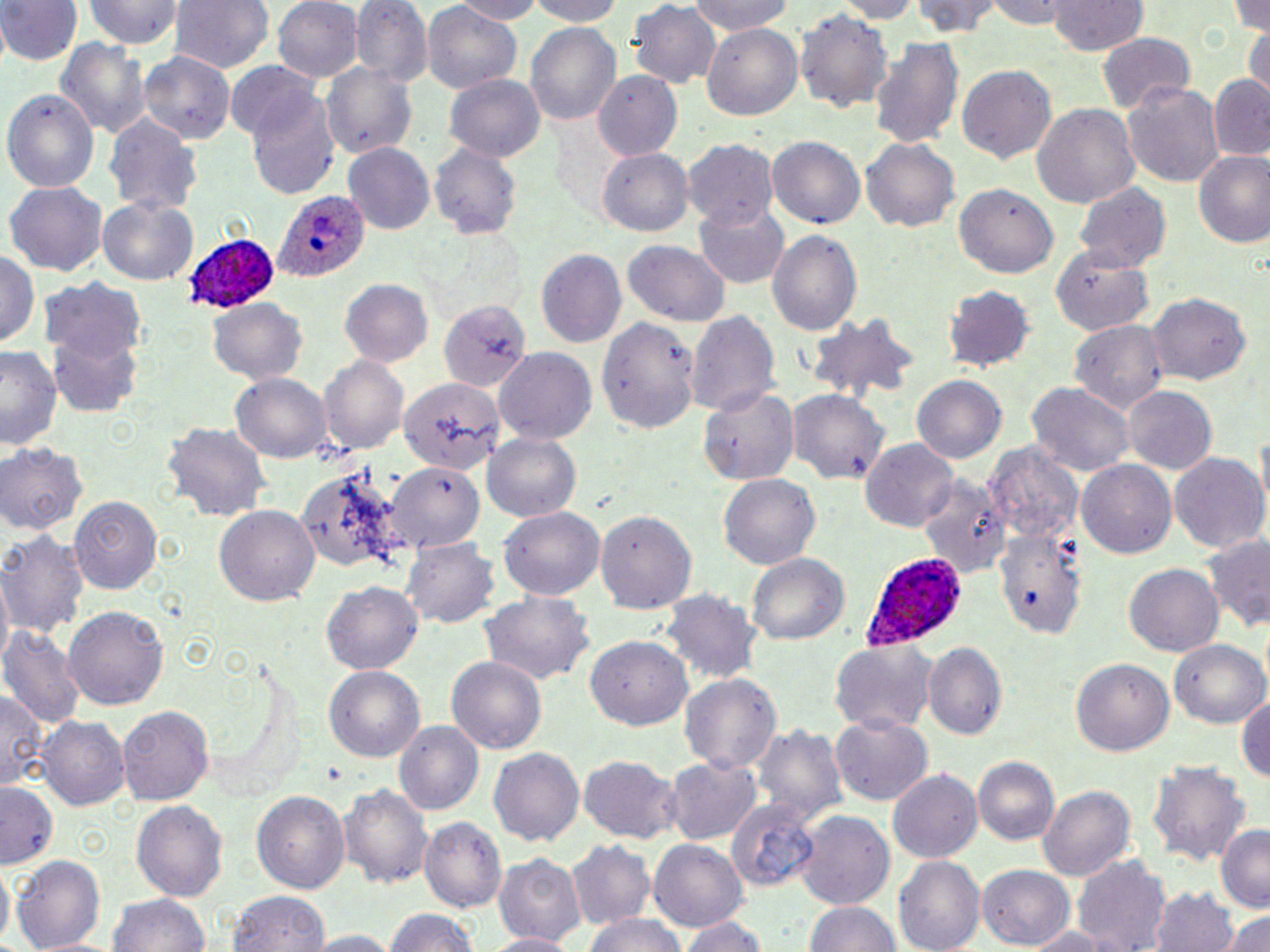
{
  "slide_level_diagnosis": "Plasmodium ovale",
  "field_of_view": "one of a larger specimen",
  "stain": "May-Grünwald-Giemsa",
  "uninfected_red_blood_cell_locations": "approximate bounding boxes as named x1/y1/x2/y2 corners in pixels: (x1=0, y1=0, x2=81, y2=67), (x1=171, y1=0, x2=274, y2=76), (x1=272, y1=0, x2=364, y2=85), (x1=351, y1=0, x2=432, y2=90), (x1=449, y1=0, x2=550, y2=23), (x1=525, y1=0, x2=632, y2=25), (x1=687, y1=0, x2=797, y2=35), (x1=828, y1=0, x2=925, y2=22), (x1=912, y1=0, x2=1003, y2=36), (x1=978, y1=0, x2=1072, y2=27), (x1=1049, y1=0, x2=1148, y2=57), (x1=1230, y1=0, x2=1270, y2=36), (x1=83, y1=1, x2=180, y2=50), (x1=422, y1=1, x2=522, y2=94), (x1=629, y1=1, x2=721, y2=91), (x1=794, y1=8, x2=894, y2=112), (x1=526, y1=22, x2=621, y2=123), (x1=1245, y1=23, x2=1270, y2=95), (x1=703, y1=25, x2=803, y2=119), (x1=1095, y1=33, x2=1196, y2=116), (x1=869, y1=36, x2=965, y2=150), (x1=56, y1=38, x2=153, y2=142), (x1=139, y1=50, x2=236, y2=144), (x1=226, y1=63, x2=325, y2=146), (x1=322, y1=65, x2=417, y2=158), (x1=957, y1=66, x2=1057, y2=164), (x1=594, y1=70, x2=681, y2=160), (x1=446, y1=73, x2=546, y2=161), (x1=1209, y1=77, x2=1270, y2=161), (x1=245, y1=82, x2=339, y2=199), (x1=1123, y1=83, x2=1226, y2=186), (x1=4, y1=89, x2=99, y2=194), (x1=1031, y1=102, x2=1140, y2=212), (x1=106, y1=115, x2=203, y2=217), (x1=766, y1=138, x2=864, y2=229), (x1=861, y1=138, x2=959, y2=230), (x1=683, y1=140, x2=776, y2=226), (x1=428, y1=141, x2=524, y2=242), (x1=342, y1=143, x2=435, y2=236), (x1=598, y1=150, x2=691, y2=235), (x1=1192, y1=150, x2=1270, y2=251), (x1=1073, y1=181, x2=1171, y2=271), (x1=6, y1=183, x2=106, y2=276), (x1=954, y1=184, x2=1058, y2=278), (x1=694, y1=197, x2=789, y2=287), (x1=99, y1=199, x2=197, y2=285), (x1=769, y1=228, x2=862, y2=338), (x1=622, y1=239, x2=730, y2=325), (x1=0, y1=247, x2=38, y2=352), (x1=1051, y1=249, x2=1152, y2=335), (x1=536, y1=250, x2=625, y2=349), (x1=41, y1=278, x2=147, y2=371), (x1=341, y1=279, x2=435, y2=368), (x1=943, y1=286, x2=1035, y2=372), (x1=1145, y1=292, x2=1252, y2=385), (x1=208, y1=297, x2=309, y2=384), (x1=437, y1=299, x2=530, y2=392), (x1=686, y1=309, x2=779, y2=416), (x1=598, y1=315, x2=695, y2=433), (x1=807, y1=316, x2=919, y2=407), (x1=1071, y1=320, x2=1169, y2=415), (x1=48, y1=333, x2=142, y2=417), (x1=0, y1=346, x2=64, y2=453), (x1=494, y1=347, x2=597, y2=442), (x1=321, y1=356, x2=409, y2=456), (x1=232, y1=373, x2=331, y2=464), (x1=912, y1=376, x2=1007, y2=466), (x1=398, y1=379, x2=505, y2=478), (x1=1027, y1=382, x2=1134, y2=477), (x1=1122, y1=384, x2=1216, y2=475), (x1=700, y1=388, x2=801, y2=485), (x1=788, y1=389, x2=887, y2=483), (x1=164, y1=420, x2=269, y2=526), (x1=481, y1=430, x2=582, y2=521), (x1=861, y1=439, x2=958, y2=533), (x1=0, y1=442, x2=88, y2=532), (x1=1169, y1=451, x2=1269, y2=554), (x1=1078, y1=460, x2=1177, y2=559), (x1=386, y1=462, x2=485, y2=550), (x1=297, y1=464, x2=402, y2=574), (x1=919, y1=473, x2=1008, y2=578), (x1=717, y1=474, x2=820, y2=568), (x1=70, y1=497, x2=162, y2=595), (x1=213, y1=504, x2=318, y2=605), (x1=597, y1=507, x2=693, y2=613), (x1=501, y1=508, x2=604, y2=601), (x1=991, y1=526, x2=1086, y2=642), (x1=0, y1=528, x2=89, y2=641), (x1=1200, y1=535, x2=1270, y2=632), (x1=403, y1=538, x2=500, y2=630), (x1=748, y1=554, x2=847, y2=648), (x1=1124, y1=563, x2=1226, y2=657), (x1=1, y1=573, x2=15, y2=672), (x1=323, y1=579, x2=424, y2=675), (x1=662, y1=590, x2=758, y2=686), (x1=481, y1=591, x2=594, y2=686), (x1=64, y1=604, x2=167, y2=712), (x1=2, y1=627, x2=84, y2=730), (x1=586, y1=634, x2=694, y2=727), (x1=829, y1=638, x2=939, y2=736), (x1=1170, y1=639, x2=1270, y2=729), (x1=923, y1=644, x2=1006, y2=742), (x1=447, y1=656, x2=546, y2=753), (x1=1070, y1=656, x2=1173, y2=755), (x1=325, y1=665, x2=425, y2=760), (x1=679, y1=671, x2=783, y2=774), (x1=0, y1=688, x2=43, y2=792), (x1=1237, y1=690, x2=1270, y2=788), (x1=119, y1=706, x2=213, y2=808), (x1=832, y1=711, x2=931, y2=804), (x1=38, y1=717, x2=128, y2=809), (x1=755, y1=721, x2=845, y2=830), (x1=392, y1=722, x2=483, y2=817), (x1=487, y1=746, x2=585, y2=847), (x1=580, y1=756, x2=680, y2=843), (x1=665, y1=756, x2=760, y2=848), (x1=1147, y1=756, x2=1250, y2=866), (x1=972, y1=757, x2=1061, y2=848), (x1=889, y1=768, x2=984, y2=864), (x1=340, y1=780, x2=435, y2=892), (x1=0, y1=782, x2=61, y2=868), (x1=1039, y1=785, x2=1135, y2=882), (x1=252, y1=791, x2=349, y2=891), (x1=133, y1=799, x2=227, y2=903), (x1=726, y1=800, x2=822, y2=892), (x1=795, y1=811, x2=894, y2=907), (x1=422, y1=818, x2=506, y2=915), (x1=1217, y1=826, x2=1270, y2=912), (x1=647, y1=838, x2=750, y2=934), (x1=568, y1=839, x2=656, y2=931), (x1=496, y1=853, x2=587, y2=946), (x1=12, y1=854, x2=104, y2=952), (x1=1073, y1=857, x2=1172, y2=951), (x1=894, y1=858, x2=985, y2=950), (x1=978, y1=863, x2=1076, y2=948), (x1=0, y1=867, x2=14, y2=944), (x1=1150, y1=886, x2=1241, y2=952), (x1=228, y1=891, x2=330, y2=952), (x1=108, y1=894, x2=213, y2=952), (x1=802, y1=899, x2=903, y2=952), (x1=1221, y1=907, x2=1270, y2=952), (x1=381, y1=910, x2=484, y2=952), (x1=679, y1=913, x2=771, y2=952), (x1=583, y1=915, x2=690, y2=952), (x1=1018, y1=925, x2=1116, y2=950), (x1=307, y1=931, x2=395, y2=952), (x1=481, y1=931, x2=580, y2=952)",
  "magnification": "1000x",
  "modality": "light microscopy",
  "image_size": "1270×952 pixels",
  "plasmodium_ovale_infected_red_blood_cell_locations": "approximate bounding boxes as named x1/y1/x2/y2 corners in pixels: (x1=275, y1=191, x2=367, y2=282), (x1=181, y1=233, x2=275, y2=314), (x1=861, y1=551, x2=965, y2=650)",
  "preparation": "thin blood smear"
}